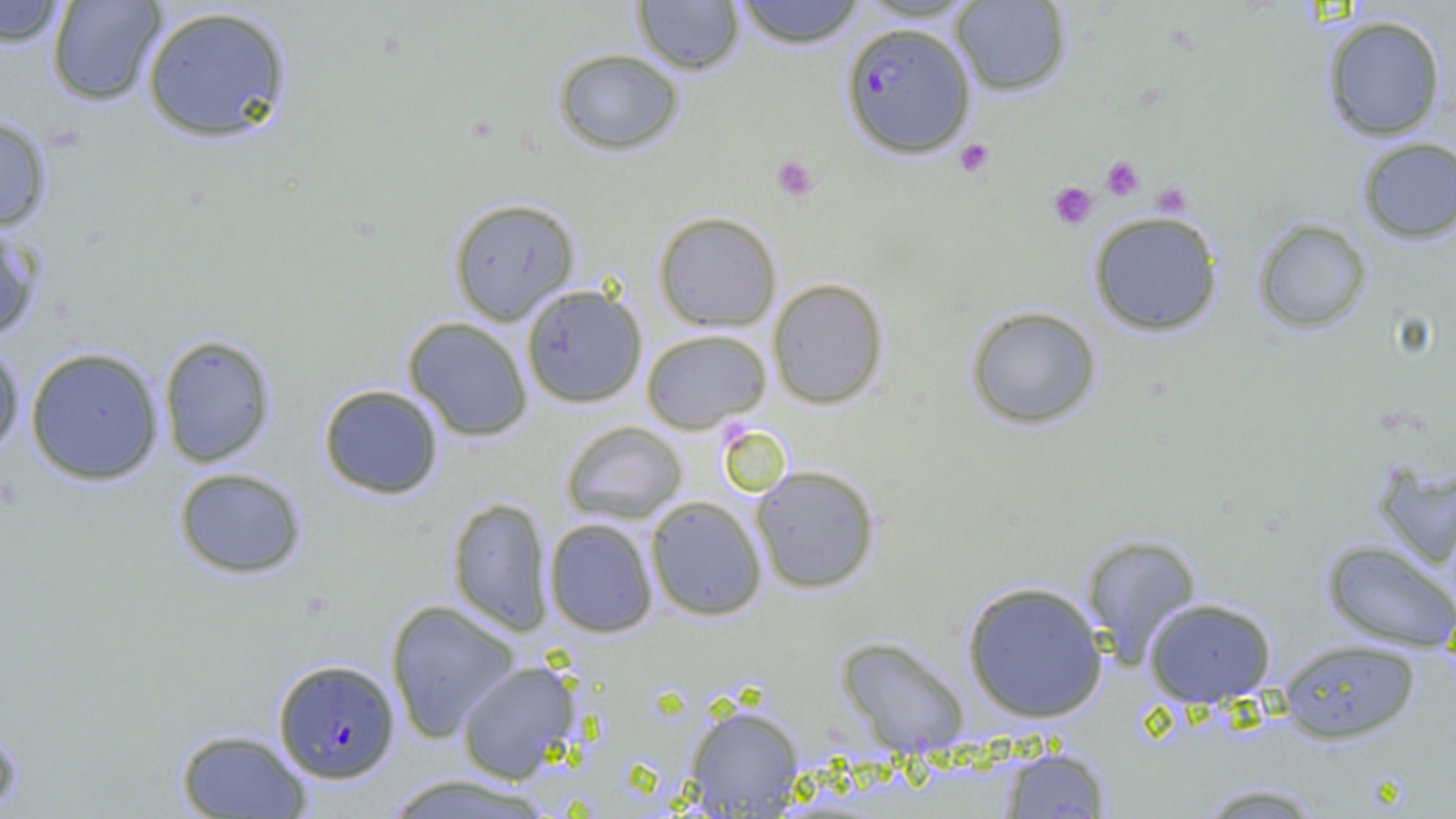

Summary:
  - Coordinate format: approximate bounding boxes as named x1/y1/x2/y2 corners in pixels
  - Platelet locations: (x1=954, y1=138, x2=995, y2=178), (x1=771, y1=155, x2=818, y2=201), (x1=1101, y1=156, x2=1144, y2=200), (x1=1048, y1=181, x2=1098, y2=230), (x1=1152, y1=183, x2=1191, y2=217)
  - Plasmodium falciparum-infected red blood cell locations: (x1=841, y1=21, x2=975, y2=158), (x1=273, y1=658, x2=399, y2=783)
  - Uninfected red blood cell locations: (x1=46, y1=0, x2=167, y2=107), (x1=733, y1=0, x2=867, y2=48), (x1=0, y1=1, x2=70, y2=48), (x1=632, y1=1, x2=745, y2=75), (x1=950, y1=1, x2=1072, y2=96), (x1=141, y1=5, x2=293, y2=144), (x1=1322, y1=14, x2=1447, y2=141), (x1=552, y1=47, x2=684, y2=155), (x1=0, y1=113, x2=53, y2=232), (x1=1357, y1=137, x2=1456, y2=244), (x1=448, y1=197, x2=580, y2=325), (x1=1087, y1=210, x2=1224, y2=336), (x1=653, y1=211, x2=782, y2=331), (x1=1252, y1=218, x2=1373, y2=334), (x1=0, y1=219, x2=44, y2=342), (x1=767, y1=278, x2=889, y2=409), (x1=521, y1=284, x2=647, y2=408), (x1=965, y1=305, x2=1102, y2=430), (x1=403, y1=317, x2=533, y2=441), (x1=640, y1=328, x2=772, y2=433), (x1=158, y1=334, x2=277, y2=468), (x1=0, y1=339, x2=25, y2=461), (x1=25, y1=346, x2=165, y2=485), (x1=318, y1=384, x2=444, y2=500), (x1=560, y1=420, x2=688, y2=524), (x1=1370, y1=458, x2=1456, y2=570), (x1=750, y1=464, x2=881, y2=593), (x1=172, y1=467, x2=307, y2=579), (x1=645, y1=495, x2=767, y2=621), (x1=447, y1=497, x2=553, y2=635), (x1=544, y1=518, x2=658, y2=637), (x1=1081, y1=533, x2=1202, y2=665), (x1=1321, y1=540, x2=1456, y2=652), (x1=961, y1=580, x2=1109, y2=723), (x1=1143, y1=597, x2=1277, y2=707), (x1=386, y1=599, x2=521, y2=741), (x1=836, y1=636, x2=970, y2=755), (x1=1279, y1=639, x2=1421, y2=743), (x1=456, y1=660, x2=582, y2=783), (x1=683, y1=704, x2=805, y2=816), (x1=0, y1=722, x2=24, y2=818), (x1=175, y1=728, x2=313, y2=818), (x1=998, y1=745, x2=1112, y2=818), (x1=381, y1=773, x2=557, y2=818), (x1=1192, y1=781, x2=1330, y2=818)
  - Slide-level diagnosis: Plasmodium falciparum
  - Preparation: thin blood smear
  - Magnification: 1000x
  - Field of view: one of a larger specimen
  - Image size: 1456×819 pixels
  - Modality: light microscopy